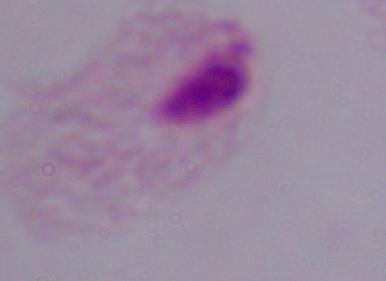

1000x magnification. A trichomonad is shown. Micrograph.